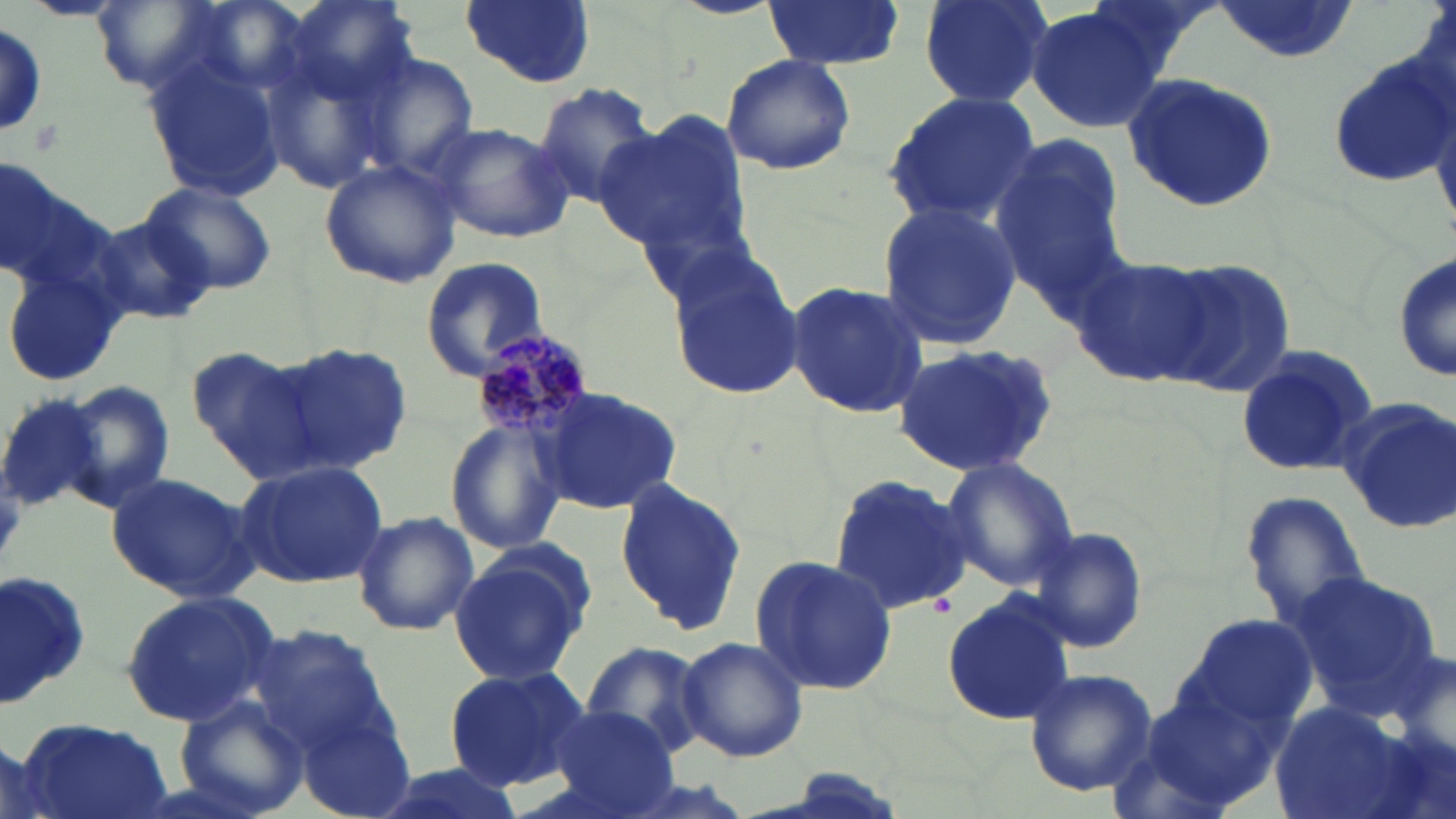

Summary:
  - Coordinate format: approximate bounding boxes as [x1, y1, x2, y2] in pixels
  - Uninfected red blood cell locations: [20, 0, 126, 20], [91, 0, 221, 92], [288, 0, 422, 103], [461, 0, 595, 88], [915, 0, 1055, 108], [1215, 0, 1360, 63], [760, 1, 906, 70], [1025, 7, 1168, 134], [0, 24, 48, 135], [356, 51, 479, 187], [1326, 51, 1456, 188], [719, 54, 857, 176], [142, 57, 287, 200], [1120, 71, 1280, 214], [532, 83, 662, 207], [878, 91, 1043, 226], [597, 110, 750, 261], [431, 121, 575, 244], [990, 136, 1128, 303], [320, 158, 463, 288], [0, 159, 85, 285], [143, 182, 276, 295], [875, 201, 1023, 351], [88, 212, 217, 326], [1394, 245, 1456, 392], [663, 247, 806, 402], [1069, 254, 1216, 388], [419, 257, 549, 379], [1156, 258, 1297, 397], [3, 265, 125, 392], [782, 279, 930, 422], [277, 342, 413, 473], [890, 344, 1061, 475], [188, 345, 322, 474], [1232, 345, 1380, 478], [63, 379, 176, 511], [539, 385, 682, 516], [0, 391, 110, 513], [1336, 398, 1456, 536], [445, 418, 567, 557], [233, 457, 389, 589], [941, 457, 1078, 591], [106, 471, 259, 604], [827, 474, 973, 616], [612, 476, 751, 637], [1242, 491, 1373, 628], [352, 511, 478, 636], [1025, 524, 1154, 654], [448, 543, 595, 688], [751, 554, 897, 697], [0, 567, 96, 711], [1288, 569, 1445, 720], [119, 591, 279, 725], [941, 593, 1076, 724], [1177, 615, 1318, 736], [247, 623, 393, 757], [678, 637, 809, 762], [581, 643, 707, 758], [443, 664, 590, 791], [1021, 668, 1157, 796], [174, 694, 309, 819], [1267, 700, 1426, 819], [543, 705, 679, 819], [296, 706, 413, 818], [17, 714, 174, 819], [0, 735, 51, 819], [359, 760, 532, 819]
  - Plasmodium malariae-infected red blood cell locations: [468, 331, 599, 452]
  - Slide-level diagnosis: Plasmodium malariae
  - Preparation: thin blood film
  - Image size: 1456×819 pixels
  - Stain: May-Grünwald-Giemsa
  - Magnification: 1000x
  - Field of view: single
  - Modality: light microscopy